Give the position of every leukocyte.
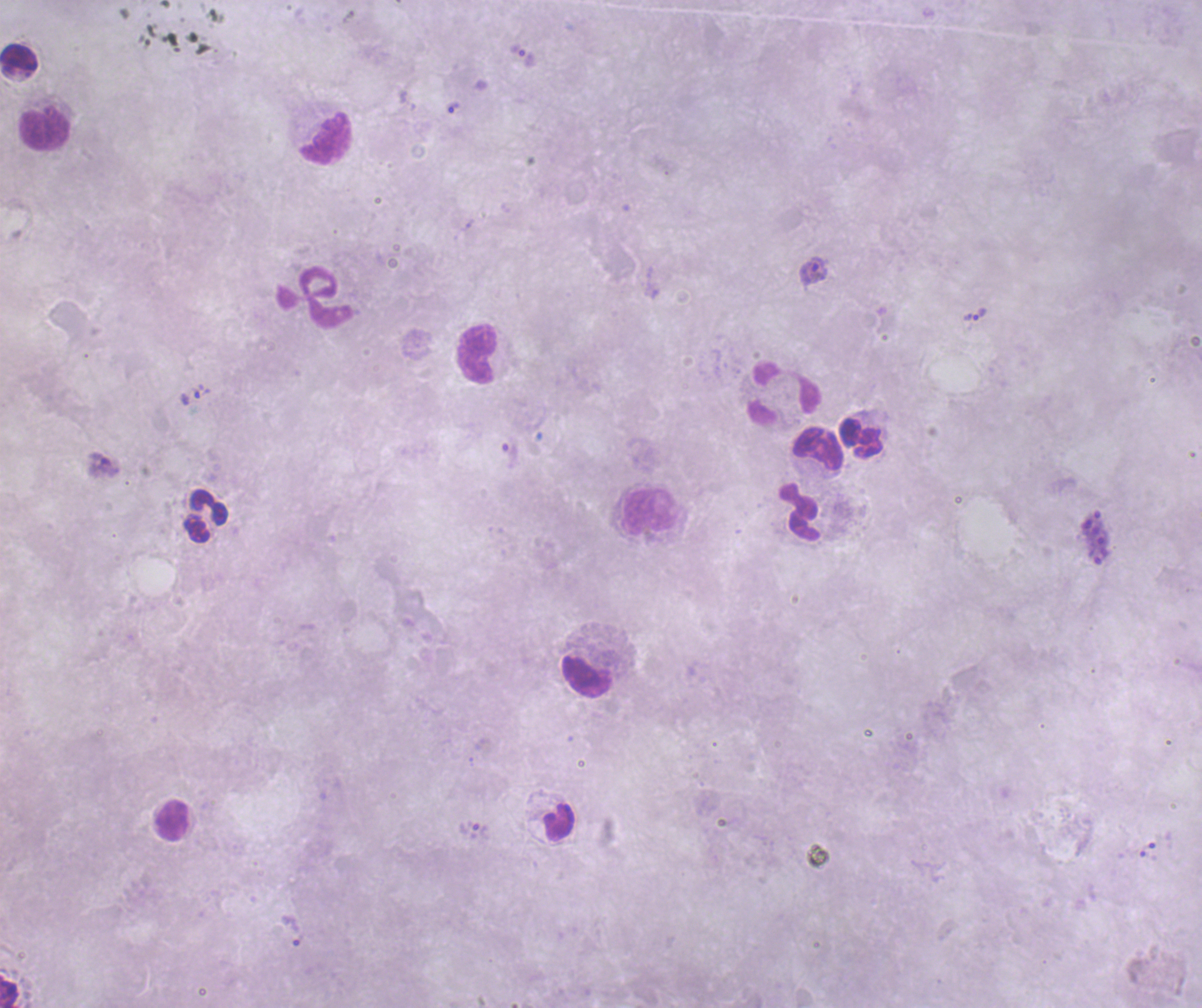

Approximate centers as (x, y) in pixels.
Leukocytes: (18, 57), (44, 128), (326, 138), (314, 297), (477, 353), (786, 393), (861, 439), (818, 448), (648, 511), (800, 513), (205, 515), (586, 676), (171, 820), (559, 822), (9, 992).

Approximate centers as (x, y) in pixels. Schizont locations: (1095, 538). Trophozoite locations: (453, 107), (813, 270), (974, 314), (195, 394), (510, 455), (481, 832), (292, 932). Life-cycle stages observed: trophozoite, schizont. Captured at 100x magnification. Result: malaria parasites detected. Coloration quality: bad. Thick blood smear. Single field of view. Background quality: poor. Romanowsky-stained preparation. Previously used in an actual diagnosis. Image is 1202×1008 pixels.